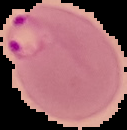 Result: Plasmodium parasites identified. From a thin blood film. Image is 127×130 pixels. Cell region segmented out of the field of view; the surrounding area is masked to black.